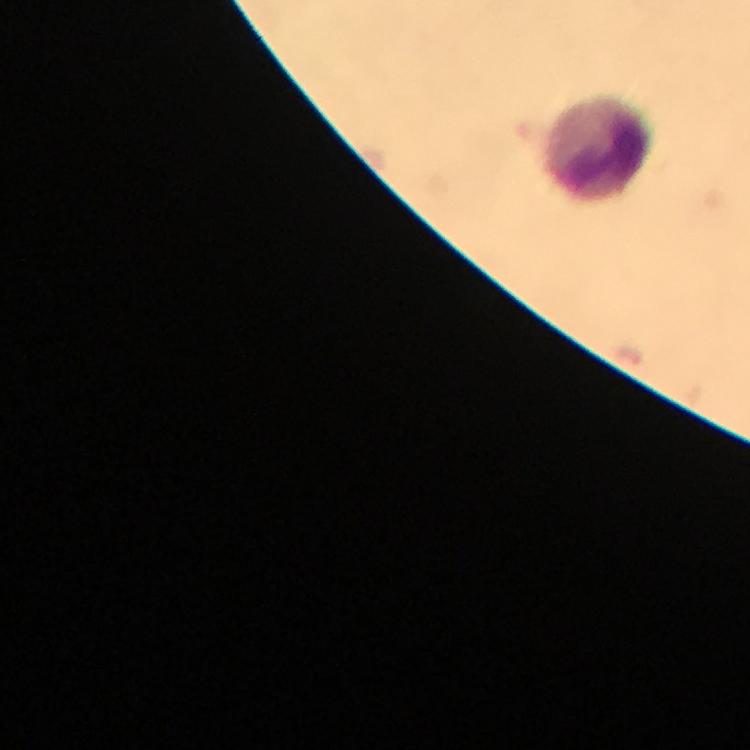

stain: Giemsa
immersion_oil: applied
context: from a malaria diagnostic workup
image_size: 750×750 pixels
malaria_parasites: none detected
preparation: thick blood film
leukocyte_locations: 'approximate centers as (x, y) in pixels: (600, 147)'
cropped_from: one field of view
magnification: 100x
capture: smartphone camera through the microscope